Locate and identify every blood parasite.
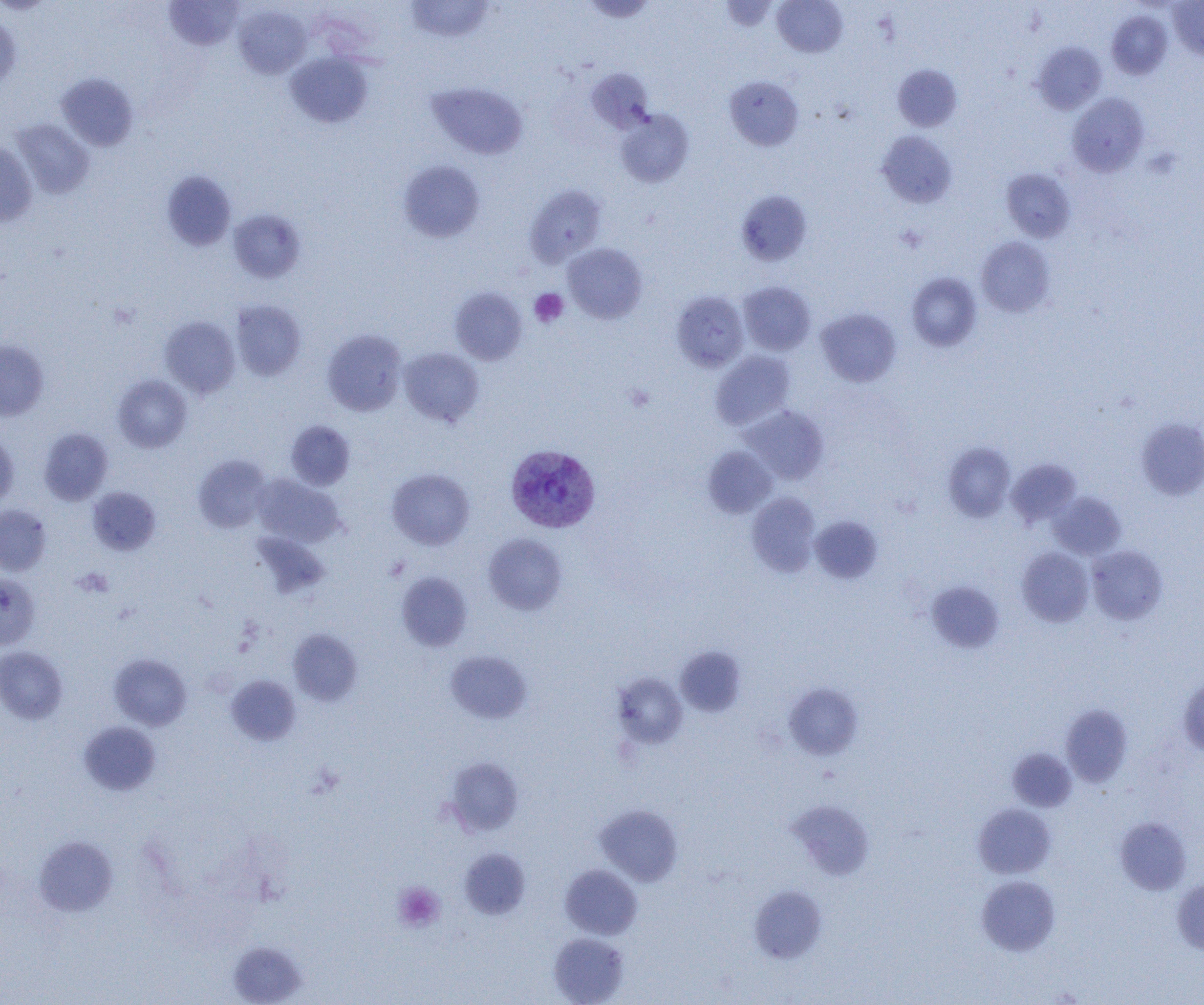
Approximate bounding boxes as named x1/y1/x2/y2 corners in pixels.
Plasmodium vivax-infected red blood cells: (x1=505, y1=444, x2=600, y2=533).
No Plasmodium falciparum, Plasmodium ovale, Plasmodium malariae, Babesia divergens, or Trypanosoma brucei observed.

Summary:
  - Platelet locations: (x1=896, y1=224, x2=927, y2=253), (x1=529, y1=289, x2=568, y2=327), (x1=625, y1=383, x2=655, y2=412), (x1=75, y1=567, x2=112, y2=597), (x1=392, y1=882, x2=445, y2=932)
  - Uninfected red blood cell locations: (x1=163, y1=0, x2=244, y2=50), (x1=406, y1=0, x2=494, y2=42), (x1=580, y1=0, x2=658, y2=22), (x1=720, y1=0, x2=779, y2=31), (x1=772, y1=0, x2=847, y2=57), (x1=1168, y1=0, x2=1204, y2=60), (x1=233, y1=4, x2=311, y2=79), (x1=1106, y1=11, x2=1173, y2=80), (x1=0, y1=12, x2=20, y2=93), (x1=1033, y1=42, x2=1106, y2=114), (x1=285, y1=52, x2=372, y2=128), (x1=893, y1=64, x2=962, y2=131), (x1=586, y1=68, x2=654, y2=134), (x1=56, y1=73, x2=139, y2=151), (x1=724, y1=76, x2=803, y2=151), (x1=426, y1=82, x2=528, y2=160), (x1=1067, y1=93, x2=1149, y2=176), (x1=615, y1=109, x2=694, y2=187), (x1=11, y1=119, x2=95, y2=199), (x1=877, y1=130, x2=957, y2=208), (x1=0, y1=142, x2=37, y2=226), (x1=398, y1=160, x2=485, y2=243), (x1=1001, y1=169, x2=1075, y2=242), (x1=161, y1=170, x2=236, y2=251), (x1=525, y1=185, x2=607, y2=266), (x1=736, y1=189, x2=812, y2=266), (x1=228, y1=209, x2=306, y2=283), (x1=977, y1=237, x2=1054, y2=317), (x1=563, y1=243, x2=647, y2=323), (x1=906, y1=272, x2=982, y2=352), (x1=738, y1=281, x2=815, y2=355), (x1=450, y1=287, x2=527, y2=365), (x1=671, y1=291, x2=749, y2=371), (x1=230, y1=299, x2=306, y2=381), (x1=816, y1=308, x2=901, y2=386), (x1=160, y1=316, x2=240, y2=399), (x1=322, y1=329, x2=407, y2=416), (x1=0, y1=340, x2=49, y2=421), (x1=399, y1=347, x2=484, y2=427), (x1=711, y1=351, x2=795, y2=429), (x1=113, y1=375, x2=192, y2=452), (x1=743, y1=405, x2=828, y2=485), (x1=1136, y1=419, x2=1204, y2=500), (x1=286, y1=421, x2=355, y2=490), (x1=39, y1=427, x2=113, y2=505), (x1=0, y1=431, x2=18, y2=509), (x1=942, y1=442, x2=1016, y2=521), (x1=703, y1=446, x2=776, y2=517), (x1=193, y1=455, x2=272, y2=533), (x1=1007, y1=458, x2=1082, y2=527), (x1=387, y1=468, x2=475, y2=550), (x1=253, y1=475, x2=345, y2=547), (x1=87, y1=486, x2=161, y2=555), (x1=746, y1=492, x2=821, y2=577), (x1=1050, y1=492, x2=1126, y2=560), (x1=0, y1=504, x2=52, y2=575), (x1=809, y1=515, x2=883, y2=584), (x1=252, y1=531, x2=329, y2=598), (x1=483, y1=533, x2=567, y2=615), (x1=1087, y1=545, x2=1167, y2=625), (x1=1016, y1=547, x2=1094, y2=626), (x1=396, y1=571, x2=472, y2=651), (x1=0, y1=573, x2=40, y2=650), (x1=926, y1=581, x2=1004, y2=653), (x1=288, y1=629, x2=363, y2=705), (x1=0, y1=646, x2=68, y2=724), (x1=676, y1=646, x2=746, y2=717), (x1=445, y1=650, x2=532, y2=723), (x1=108, y1=653, x2=192, y2=730), (x1=612, y1=673, x2=688, y2=749), (x1=226, y1=675, x2=301, y2=746), (x1=1178, y1=675, x2=1204, y2=757), (x1=782, y1=682, x2=863, y2=760), (x1=1061, y1=704, x2=1133, y2=787), (x1=78, y1=722, x2=161, y2=796), (x1=1008, y1=748, x2=1077, y2=812), (x1=445, y1=757, x2=523, y2=836), (x1=787, y1=799, x2=875, y2=881), (x1=595, y1=803, x2=683, y2=886), (x1=973, y1=803, x2=1056, y2=878), (x1=1114, y1=817, x2=1191, y2=895), (x1=34, y1=835, x2=118, y2=916), (x1=459, y1=848, x2=530, y2=919), (x1=560, y1=864, x2=643, y2=939), (x1=976, y1=875, x2=1060, y2=956), (x1=1171, y1=878, x2=1204, y2=955), (x1=749, y1=886, x2=827, y2=964), (x1=548, y1=932, x2=629, y2=1005), (x1=228, y1=941, x2=308, y2=1005)
  - Slide-level diagnosis: Plasmodium vivax
  - Magnification: 1000x
  - Image size: 1204×1005 pixels
  - Field of view: one of a larger specimen
  - Preparation: thin blood smear
  - Modality: optical microscopy